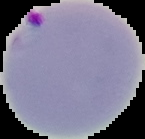

Summary:
  - Malaria status: parasitized
  - Image size: 145×139 pixels
  - Image type: cell region segmented out of the field of view; surrounding area masked to black
  - Preparation: thin blood smear